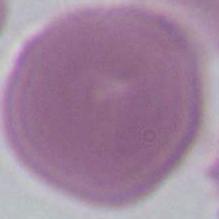
A red blood cell is seen. Captured at 1000x magnification. Photomicrograph.